Classify this cell by malaria status.
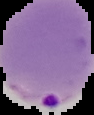
It is parasitized.

image_size: 94×115 pixels
image_type: segmented cell region on a black background
preparation: thin blood film